Classify this cell by malaria status.
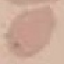
It is uninfected.

preparation = thin blood smear
image type = cell patch, automatically extracted from a larger field of view and resized to 64 × 64 pixels
capture = smartphone through the microscope eyepiece
stain = Giemsa